Classify this cell by malaria status.
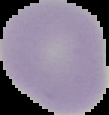

Uninfected.

From a thin blood smear. Cell region segmented out of the field of view; the surrounding area is masked to black. Image is 109×115 pixels.